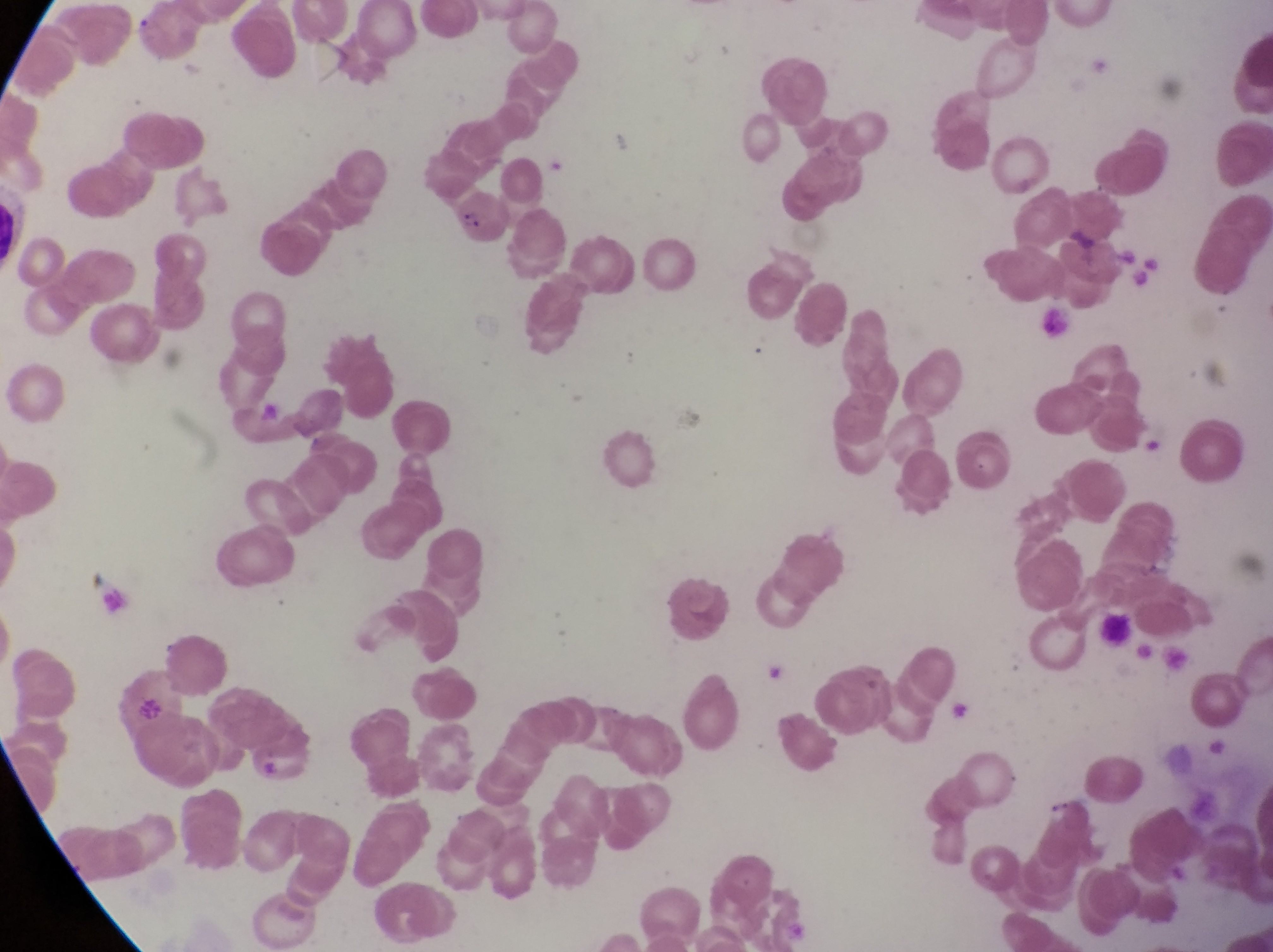 Approximate bounding boxes as {left, top, right, bottom} in pixels. Parasitised red blood cell locations: {452, 190, 515, 250}. Photographed through the eyepiece of an Olympus CX-23 microscope with a smartphone camera. Magnification of 1000x. Collected in Uganda. Image is 1273×952 pixels. Single field of view. Thin blood smear.